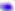

modality = photomicrograph
identification = Toxoplasma gondii
magnification = 400x